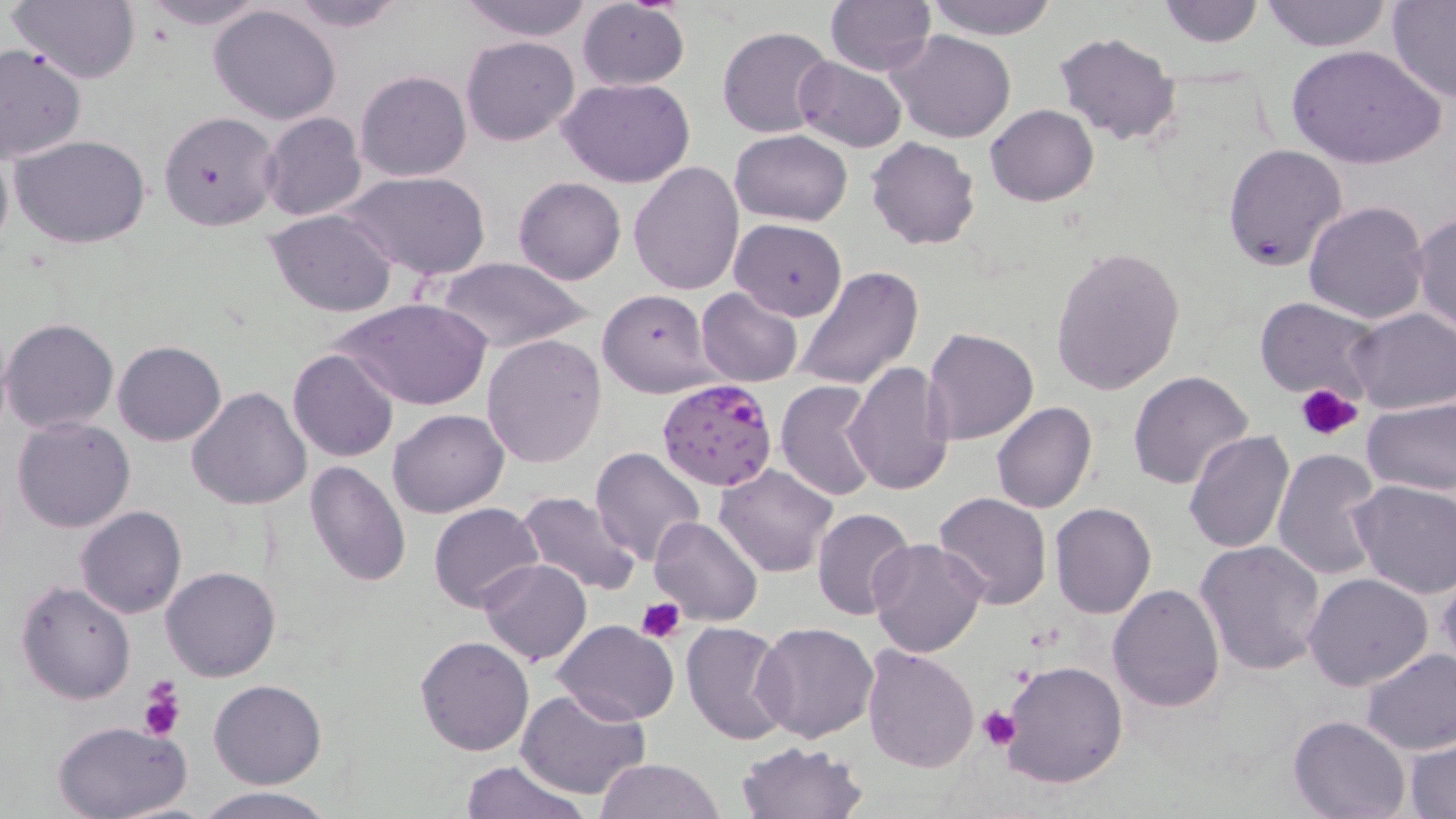

Summary:
  - Coordinate format: approximate bounding boxes as (x1,y1)-(x2,y2) corner pairs in pixels
  - Platelet locations: (1294,383)-(1364,443), (635,598)-(686,642), (136,676)-(186,744), (981,709)-(1019,749)
  - Plasmodium falciparum-infected red blood cell locations: (657,379)-(780,492)
  - Uninfected red blood cell locations: (9,0)-(141,85), (136,0)-(273,30), (279,0)-(410,33), (456,0)-(596,41), (825,0)-(936,74), (922,0)-(1058,40), (1260,0)-(1392,51), (1386,0)-(1456,103), (574,1)-(690,89), (1157,1)-(1267,49), (209,4)-(343,126), (717,26)-(837,138), (890,29)-(1017,143), (1053,31)-(1182,148), (461,35)-(579,146), (1287,44)-(1444,171), (0,45)-(87,162), (792,56)-(906,152), (356,70)-(471,181), (559,77)-(697,186), (985,104)-(1098,206), (158,111)-(281,232), (259,112)-(367,222), (731,130)-(852,225), (10,133)-(153,248), (0,136)-(14,264), (865,137)-(981,251), (1223,142)-(1347,271), (627,161)-(744,297), (344,171)-(492,281), (512,176)-(626,284), (1303,201)-(1430,324), (267,209)-(397,315), (1411,213)-(1456,334), (729,219)-(847,320), (1048,245)-(1185,397), (433,256)-(594,354), (796,266)-(924,391), (695,287)-(803,386), (597,288)-(716,397), (1252,296)-(1382,402), (334,297)-(490,412), (1345,308)-(1455,415), (1,318)-(120,434), (921,327)-(1038,446), (481,334)-(606,469), (113,340)-(226,446), (288,350)-(397,462), (845,363)-(956,499), (1128,371)-(1255,492), (774,380)-(880,502), (186,388)-(312,512), (1362,397)-(1456,496), (991,401)-(1098,514), (387,409)-(509,517), (966,415)-(1083,563), (11,417)-(135,534), (1184,430)-(1295,555), (591,446)-(706,567), (1271,450)-(1384,581), (304,461)-(411,588), (714,464)-(839,579), (1349,478)-(1455,599), (516,491)-(641,597), (933,491)-(1052,610), (429,502)-(545,612), (1049,503)-(1157,619), (75,506)-(187,619), (811,507)-(916,620), (649,515)-(762,625), (868,537)-(988,658), (1195,539)-(1327,675), (478,558)-(591,665), (161,566)-(281,683), (1303,572)-(1433,692), (1436,573)-(1456,674), (15,581)-(136,705), (1108,583)-(1226,712), (553,620)-(678,725), (681,620)-(793,744), (753,622)-(878,743), (416,635)-(534,756), (862,644)-(979,773), (1360,647)-(1456,755), (1000,661)-(1128,788), (208,679)-(327,788), (517,688)-(653,800), (1288,715)-(1412,819), (53,720)-(193,818), (1407,737)-(1456,817), (736,739)-(868,819), (596,757)-(725,818), (459,758)-(588,819), (194,787)-(337,819)
  - Slide-level diagnosis: Plasmodium falciparum
  - Image size: 1456×819 pixels
  - Preparation: thin blood smear
  - Magnification: 1000x
  - Modality: light microscopy
  - Stain: May-Grünwald-Giemsa
  - Field of view: single